Classify this cell by malaria status.
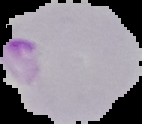

It is parasitized.

preparation = thin blood smear
image size = 142×124 pixels
image type = segmented cell region with the area outside set to black